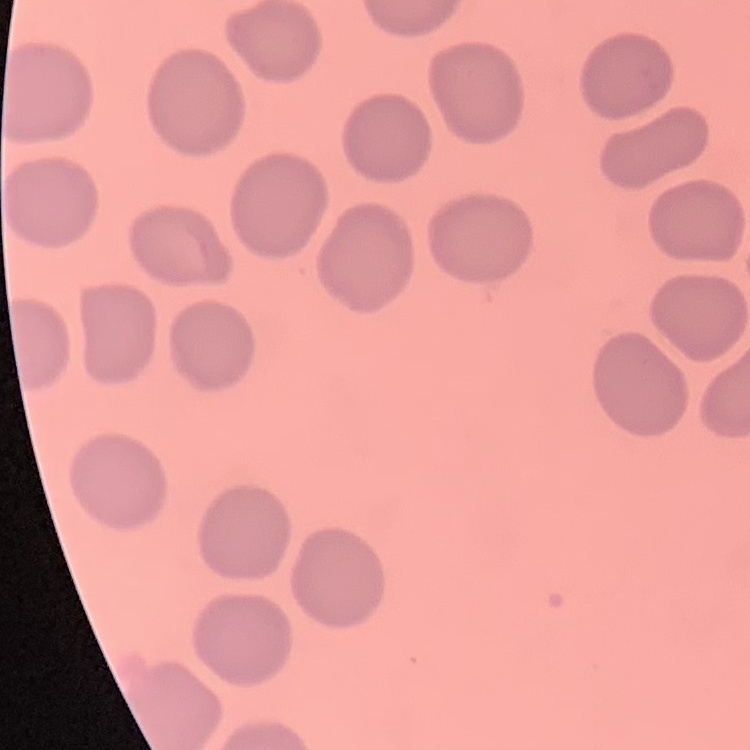
The erythrocytes show no rouleaux formation. Thin blood film. One tile cut from a larger photomicrograph. Field's or Giemsa stain.